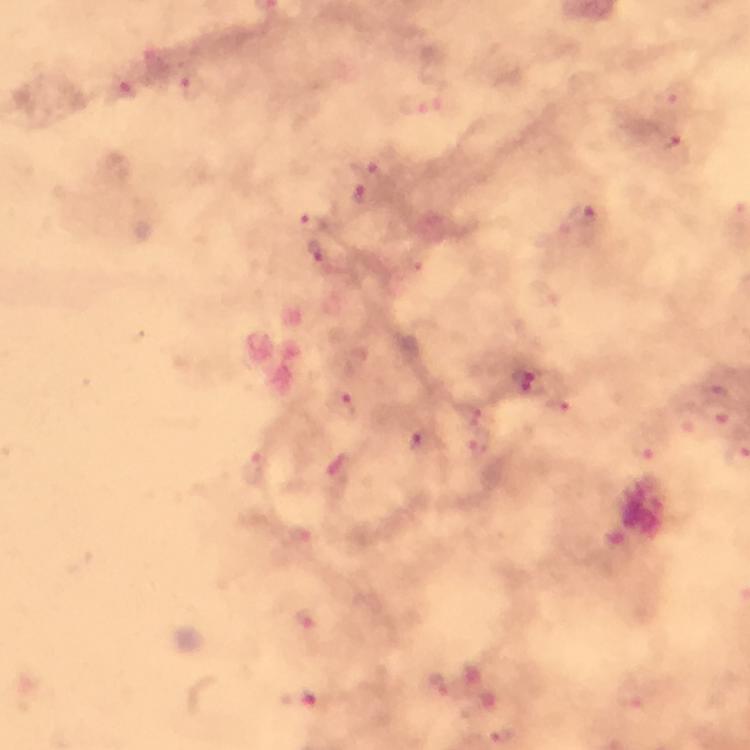

Approximate centers as {x, y} in pixels. Malaria parasite locations: {192, 85}, {127, 87}, {419, 106}, {673, 150}, {370, 167}, {362, 194}, {582, 214}, {313, 223}, {317, 251}, {415, 259}, {525, 381}, {345, 406}, {560, 410}, {473, 412}, {719, 414}, {419, 442}, {479, 446}, {647, 446}, {257, 468}, {301, 539}, {306, 620}, {441, 685}, {634, 695}, {299, 700}. A crop from one field of view. From a malaria diagnostic workup. Giemsa-stained preparation. Image is 750×750 pixels. Thick blood smear. 100x magnification. Smartphone photograph taken through a microscope. Immersion oil was used.